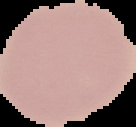
Summary:
  - Malaria status: uninfected
  - Preparation: thin blood smear
  - Image type: segmented cell region with the area outside set to black
  - Image size: 136×127 pixels